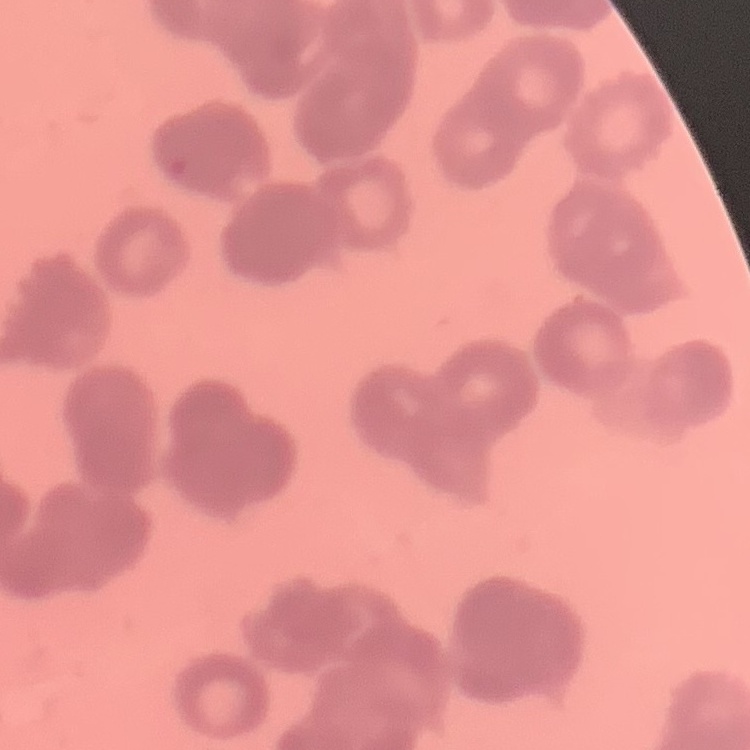
Summary:
  - Red blood cell morphology: rouleaux formation
  - Stain: Field's or Giemsa
  - Preparation: thin blood smear
  - Image type: square crop of a larger photomicrograph